Give the position of every leukocyte visible.
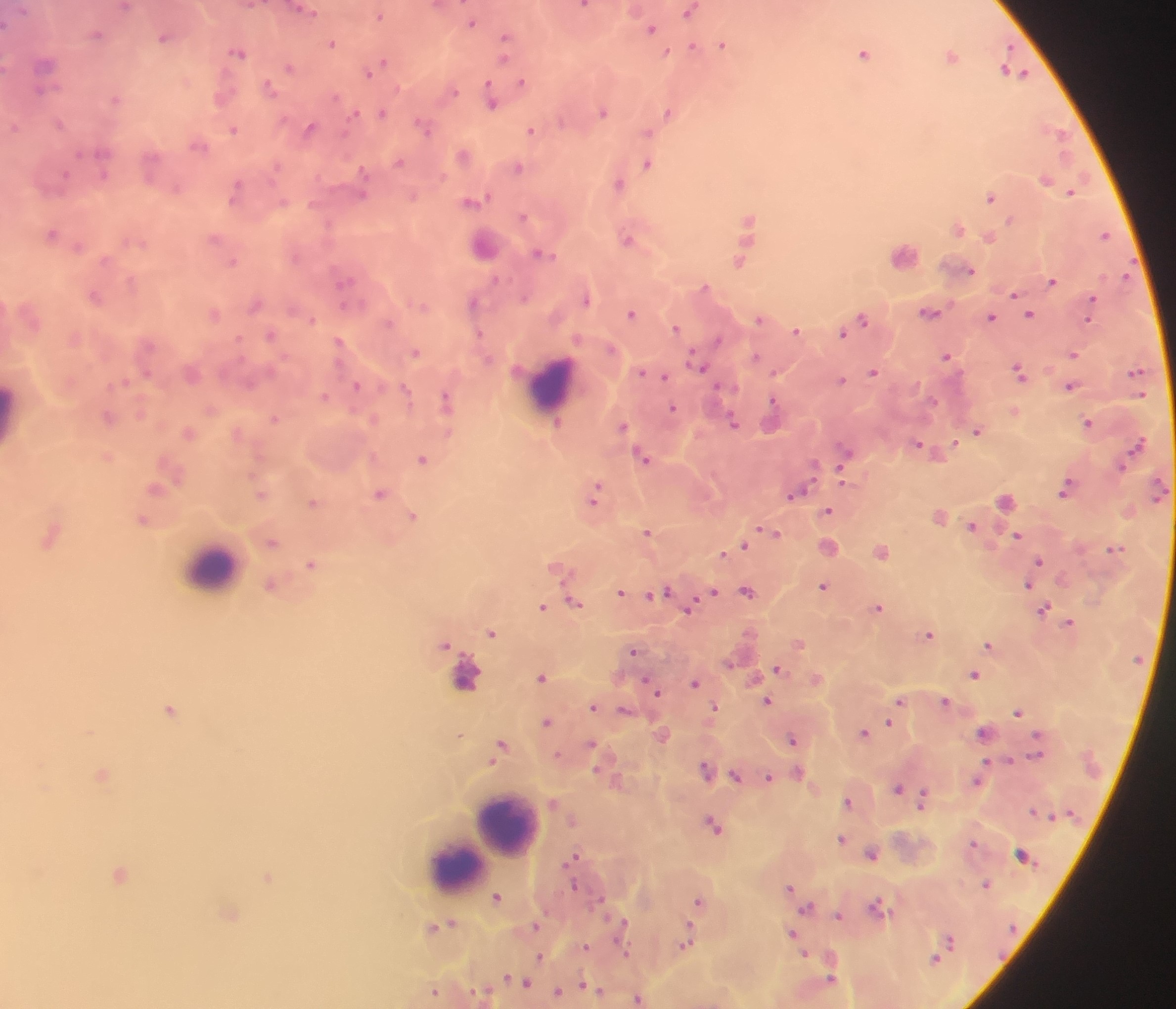
Approximate centers as (x, y) in pixels.
Leukocytes: (551, 386), (14, 413), (212, 566), (500, 824), (492, 832), (456, 861).

image size = 1176×1009 pixels
field of view = single
country = Ghana
preparation = thick blood film
capture = mobile-phone photograph through a microscope
Plasmodium parasite locations = approximate centers as (x, y) in pixels: (688, 11), (380, 15), (471, 22), (651, 28), (96, 33), (505, 36), (163, 37), (332, 42), (722, 43), (692, 46), (239, 52), (865, 52), (951, 55), (505, 58), (383, 61), (289, 66), (369, 72), (1014, 72), (521, 81), (269, 87), (399, 87), (41, 89), (454, 90), (115, 98), (491, 102), (603, 111), (668, 111), (382, 112), (60, 122), (423, 125), (14, 126), (309, 128), (234, 129), (530, 130), (1056, 131), (647, 132), (198, 145), (463, 154), (399, 161), (648, 163), (278, 166), (518, 167), (104, 171), (362, 172), (66, 175), (1045, 178), (618, 183), (176, 187), (235, 190), (1072, 191), (362, 195), (413, 196), (990, 197), (474, 199), (283, 202), (523, 215), (748, 218), (958, 227), (51, 233), (1104, 234), (990, 236), (214, 237), (627, 239), (78, 246), (541, 253), (903, 253), (739, 260), (234, 261), (969, 269), (495, 279), (345, 280), (1052, 280), (704, 286), (1014, 294), (95, 296), (524, 296), (587, 299), (1093, 299), (474, 301), (255, 304), (929, 310), (631, 313), (1030, 313), (214, 314), (992, 316), (862, 317), (1090, 317), (311, 318), (759, 318), (389, 322), (675, 327), (796, 330), (843, 332), (479, 333), (271, 334), (719, 337), (339, 340), (416, 352), (1074, 354), (756, 355), (946, 355), (697, 362), (641, 370), (1019, 370), (874, 371), (1136, 371), (665, 376), (842, 379), (123, 380), (358, 385), (1070, 385), (404, 388), (324, 396), (446, 400), (933, 400), (772, 401), (673, 407), (108, 418), (274, 418), (733, 421), (556, 422), (1088, 422), (622, 425), (977, 430), (188, 433), (918, 443), (954, 443), (1137, 443), (844, 453), (643, 457), (423, 458), (1122, 465), (813, 466), (843, 470), (155, 488), (1065, 489), (379, 492), (261, 493), (795, 493), (595, 495), (1004, 501), (313, 502), (829, 510), (413, 515), (142, 519), (971, 525), (647, 531), (772, 531), (51, 535), (1018, 535), (272, 542), (743, 545), (1114, 548), (725, 551), (882, 551), (1039, 559), (311, 564), (558, 566), (271, 584), (1028, 584), (822, 585), (665, 590), (747, 590), (621, 591), (712, 592), (573, 601), (543, 606), (689, 607), (879, 607), (1044, 609), (1069, 622), (491, 633), (929, 634), (799, 642), (445, 643), (989, 644), (633, 650), (729, 662), (778, 668), (464, 673), (974, 673), (543, 676), (695, 682), (653, 687), (900, 699), (767, 700), (945, 700), (593, 706), (714, 706), (170, 708), (624, 709), (1019, 711), (546, 721), (889, 722), (983, 731), (864, 732), (459, 734), (1036, 737), (792, 738), (592, 743), (501, 744), (1036, 753), (556, 754), (1009, 759), (986, 761), (705, 768), (595, 769), (798, 771), (102, 774), (735, 774), (769, 776), (977, 781), (897, 787), (923, 798), (848, 801), (1034, 810), (713, 823), (841, 838), (974, 842), (871, 853), (1022, 853), (573, 855), (120, 873), (268, 876), (574, 884), (986, 884), (790, 886), (497, 897), (600, 898), (697, 900), (877, 905), (807, 907), (231, 912), (838, 914), (444, 924), (536, 924), (622, 924), (688, 931), (793, 933), (950, 939), (685, 942), (587, 946), (624, 949), (803, 951), (540, 956), (934, 959), (510, 977), (830, 978), (523, 980), (583, 984), (433, 991), (558, 991), (597, 991), (638, 997)